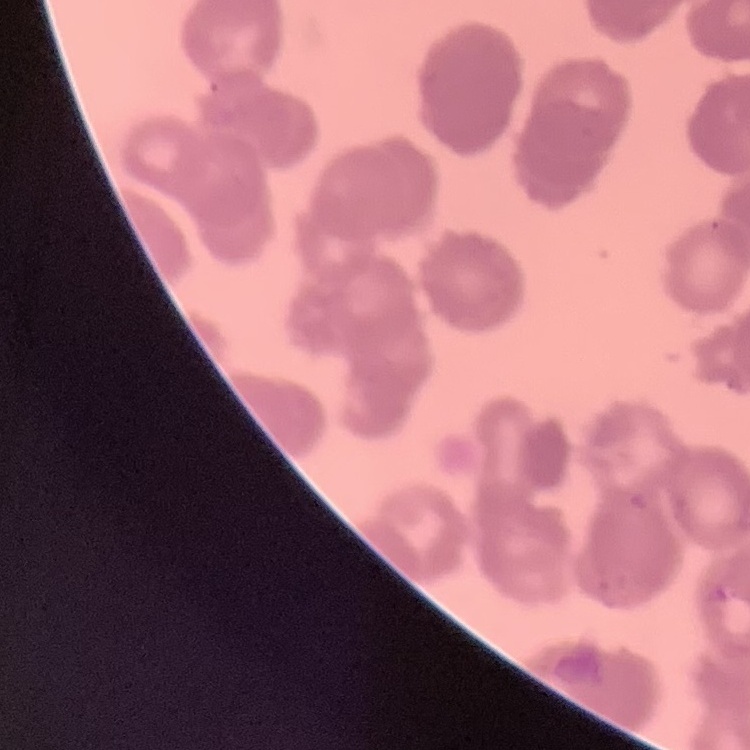

erythrocyte morphology = rouleaux formation
preparation = thin blood smear
image type = one tile cut from a larger photomicrograph
stain = Field's or Giemsa